Identify the parasite.
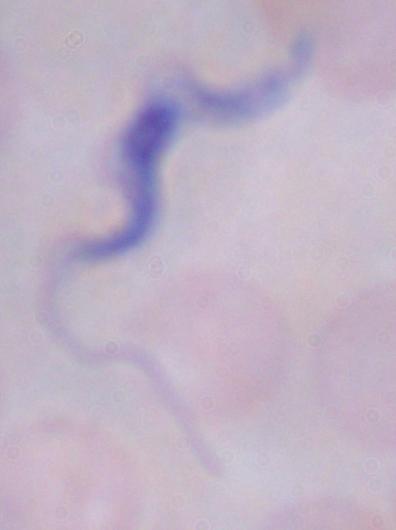
This is a trypanosome.

magnification = 1000x
modality = photomicrograph